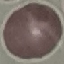 Result: no malaria parasites detected. Acquired by smartphone through the microscope eyepiece. Giemsa stain. Thin smear of blood. Cell patch, automatically extracted from a larger field of view and resized to 64 × 64 pixels.